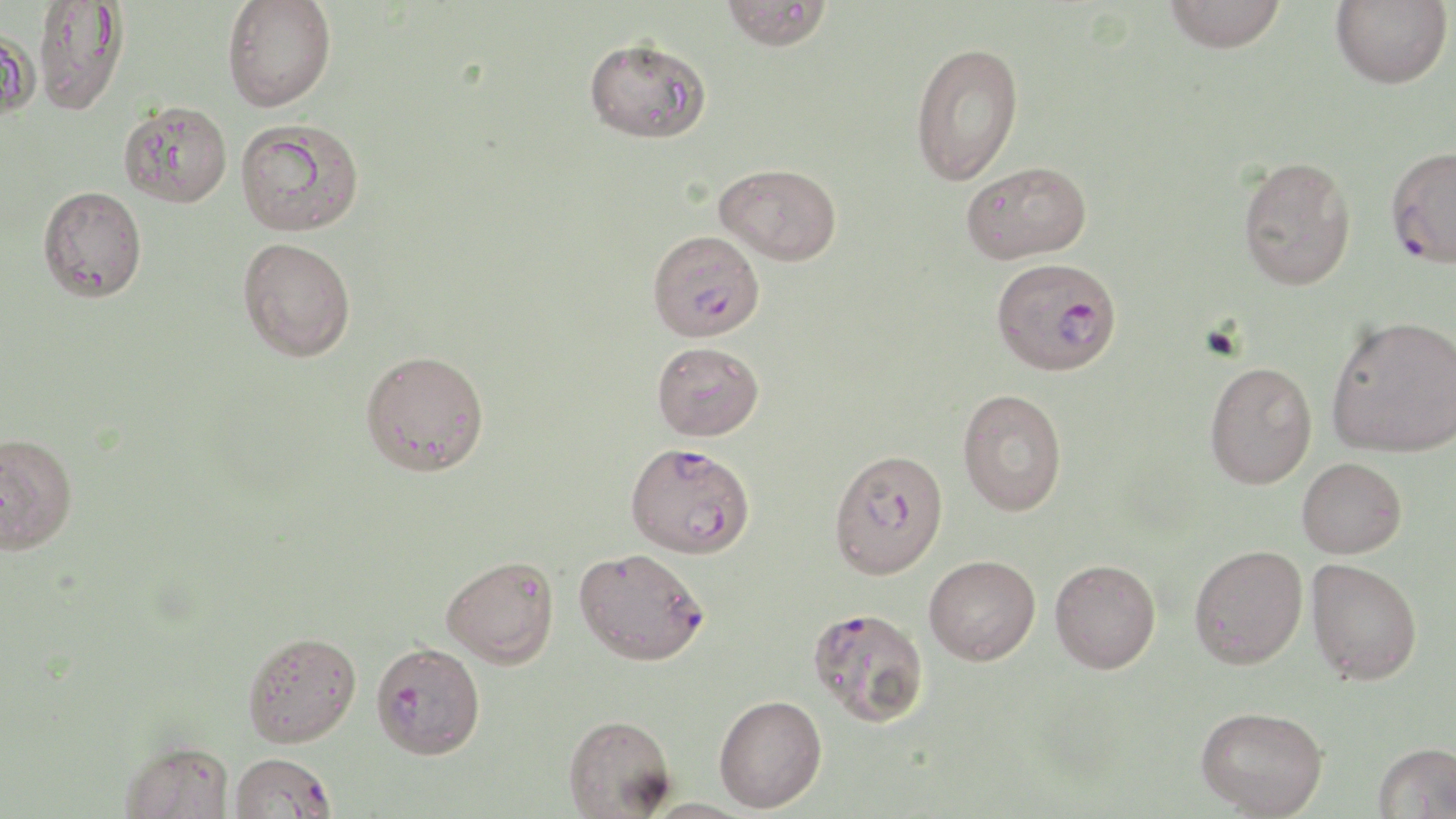

Summary:
  - Coordinate format: approximate bounding boxes as (x1, y1, x2, y2) in pixels
  - Plasmodium falciparum-infected red blood cell locations: (1385, 146, 1456, 267), (647, 229, 764, 341), (992, 256, 1122, 375), (828, 447, 949, 580), (625, 448, 759, 561), (573, 546, 710, 665), (808, 606, 930, 728), (371, 641, 486, 758), (229, 752, 336, 818)
  - Uninfected red blood cell locations: (222, 0, 336, 112), (720, 0, 833, 51), (1164, 0, 1286, 53), (1330, 0, 1452, 89), (32, 1, 129, 114), (0, 25, 40, 121), (583, 36, 711, 144), (911, 41, 1024, 185), (118, 101, 232, 207), (236, 118, 365, 236), (1238, 156, 1356, 290), (961, 160, 1091, 263), (715, 163, 842, 264), (38, 185, 147, 302), (238, 238, 356, 361), (1326, 314, 1456, 457), (652, 340, 764, 440), (360, 350, 490, 477), (1204, 361, 1317, 489), (957, 388, 1067, 516), (0, 431, 78, 555), (1297, 457, 1406, 558), (1189, 544, 1308, 669), (924, 554, 1041, 665), (442, 555, 559, 668), (1050, 558, 1160, 673), (1306, 558, 1422, 685), (243, 631, 361, 747), (714, 694, 827, 812), (1195, 705, 1328, 818), (563, 714, 676, 818), (121, 739, 234, 819), (1372, 742, 1456, 818), (640, 799, 756, 819)
  - Slide-level diagnosis: Plasmodium falciparum
  - Preparation: thin blood film
  - Stain: May-Grünwald-Giemsa
  - Image size: 1456×819 pixels
  - Modality: optical microscopy
  - Magnification: 1000x
  - Field of view: one of a larger specimen